Classify this cell by malaria status.
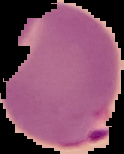
It is parasitized.

From a thin blood smear. Cell region segmented out of the field of view; the surrounding area is masked to black. Image is 124×154 pixels.